Locate every blood parasite and identify its species.
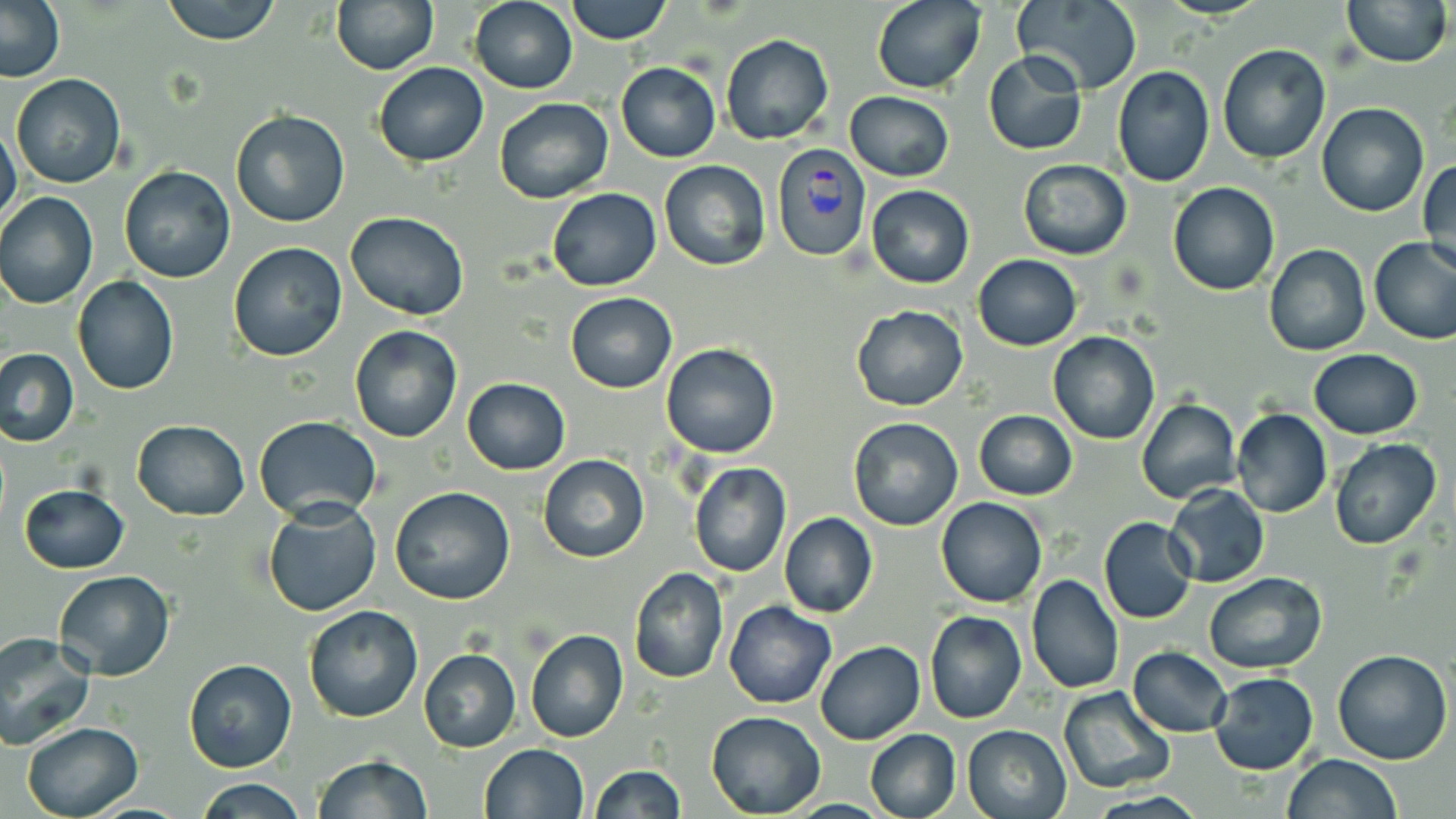

Approximate bounding boxes as [x1, y1, x2, y2] in pixels.
Plasmodium vivax-infected red blood cells: [772, 144, 871, 263].
No Plasmodium falciparum, Plasmodium ovale, Plasmodium malariae, Babesia divergens, or Trypanosoma brucei observed.

Uninfected red blood cell locations: [1, 0, 65, 83], [161, 0, 282, 45], [330, 0, 438, 74], [469, 0, 577, 93], [566, 0, 670, 45], [872, 0, 985, 93], [1011, 0, 1142, 94], [1340, 0, 1453, 69], [721, 33, 834, 145], [1218, 43, 1331, 164], [984, 51, 1088, 156], [372, 62, 489, 166], [615, 63, 721, 162], [1112, 65, 1215, 186], [10, 74, 125, 189], [846, 91, 955, 183], [493, 96, 614, 202], [1317, 103, 1430, 217], [228, 109, 350, 228], [0, 124, 23, 233], [1418, 158, 1456, 278], [1018, 159, 1131, 260], [659, 160, 771, 271], [118, 164, 235, 284], [1167, 182, 1280, 295], [867, 184, 974, 288], [547, 188, 662, 292], [1, 192, 99, 309], [347, 211, 470, 321], [1369, 238, 1456, 344], [227, 242, 349, 363], [1264, 244, 1371, 357], [973, 254, 1082, 350], [72, 276, 179, 394], [565, 291, 676, 393], [850, 304, 968, 411], [349, 324, 462, 442], [1048, 331, 1159, 445], [661, 343, 780, 457], [1, 347, 78, 446], [1308, 349, 1422, 439], [461, 377, 570, 474], [1137, 397, 1241, 504], [1231, 407, 1331, 519], [973, 409, 1077, 501], [253, 416, 383, 522], [846, 418, 964, 532], [132, 420, 249, 519], [1331, 438, 1442, 550], [538, 453, 649, 563], [688, 463, 792, 578], [19, 483, 129, 574], [1166, 485, 1270, 588], [389, 488, 515, 606], [936, 496, 1047, 607], [262, 500, 382, 618], [778, 512, 877, 617], [1098, 517, 1197, 624], [628, 567, 729, 684], [53, 570, 175, 680], [1204, 572, 1327, 673], [1027, 573, 1125, 692], [724, 601, 835, 708], [303, 604, 423, 723], [924, 612, 1027, 725], [525, 630, 628, 743], [0, 632, 96, 751], [815, 640, 924, 745], [1128, 647, 1233, 738], [418, 648, 521, 752], [1333, 649, 1453, 764], [182, 658, 297, 774], [1208, 673, 1319, 775], [1058, 685, 1174, 795], [705, 711, 826, 817], [19, 721, 144, 818], [961, 724, 1072, 818], [864, 728, 961, 819], [477, 742, 589, 819], [1282, 754, 1403, 818], [312, 755, 435, 818], [588, 764, 684, 819], [193, 778, 310, 818]. Slide-level diagnosis: Plasmodium vivax. May-Grünwald-Giemsa-stained preparation. Light microscopy. 1000x magnification. Image is 1456×819 pixels. Single field of view. Thin blood film.